Comment on the morphology of the red blood cells.
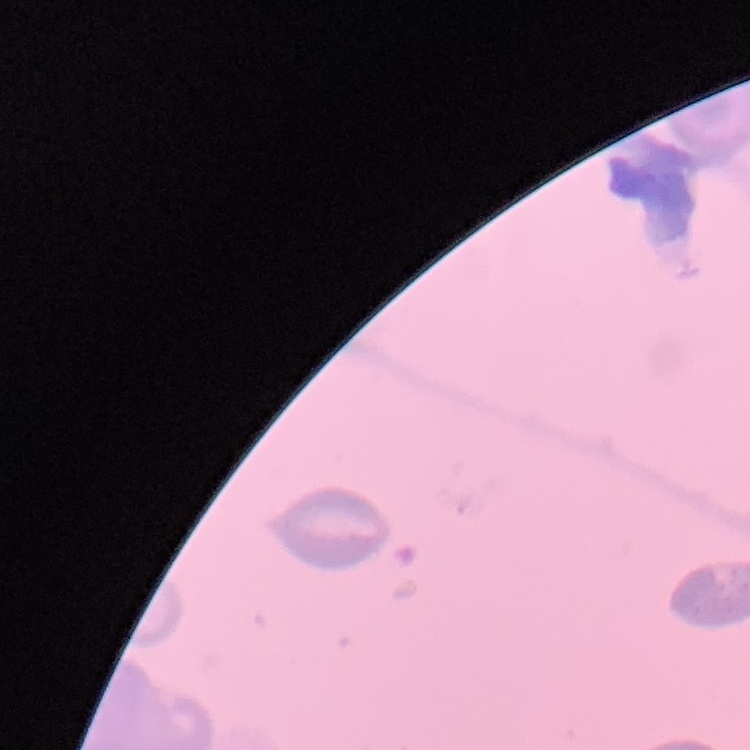
No rouleaux formation.

Summary:
  - Stain: Field's or Giemsa
  - Image type: square crop of a larger photomicrograph
  - Preparation: thin blood smear